Assess this cell for malaria.
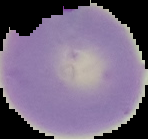

Parasitized.

Summary:
  - Image size: 148×139 pixels
  - Image type: cell region segmented out of the field of view; surrounding area masked to black
  - Preparation: thin blood smear